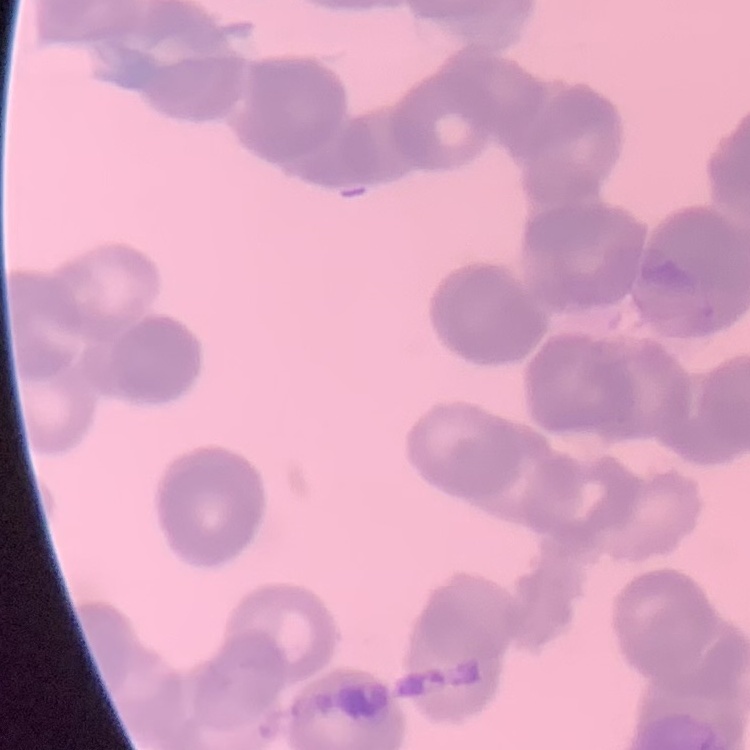 The erythrocytes show rouleaux formation. One tile cut from a larger photomicrograph. Field's or Giemsa stain. Thin blood smear.